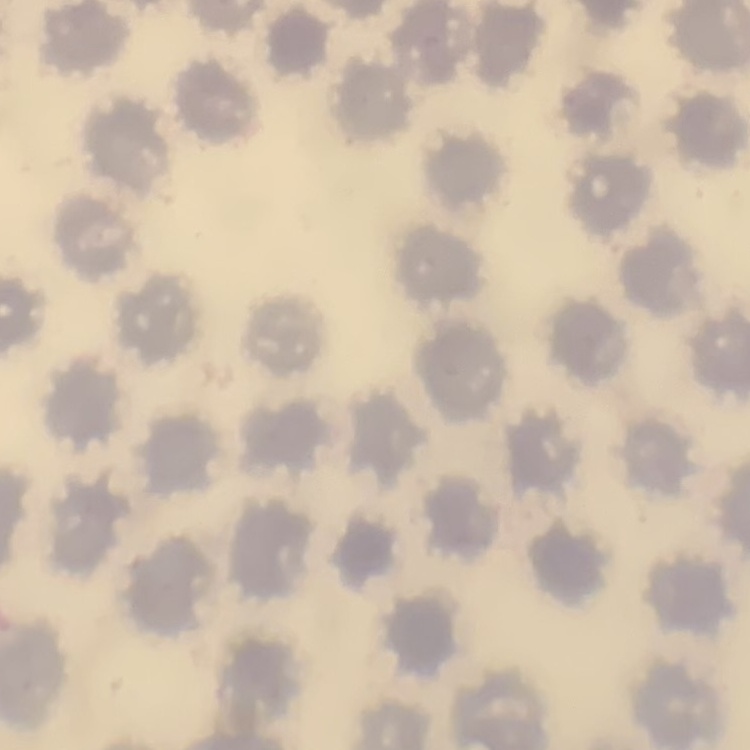 The red blood cells show no rouleaux formation. Thin blood film. One tile cut from a larger photomicrograph. Field's or Giemsa stain.